Classify this cell by malaria status.
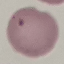

Uninfected.

Giemsa stain. Photographed with a smartphone camera at the microscope eyepiece. Cell patch, automatically extracted from a larger field of view and resized to 64 × 64 pixels. Thin smear of blood.